Report the malaria status of this cell.
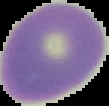

Uninfected.

preparation = thin blood film
image type = segmented cell region on a black background
image size = 109×106 pixels